Assess this cell for malaria.
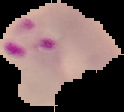

It is parasitized.

The area outside the segmented cell region is set to black. Image is 124×112 pixels. From a thin blood smear.